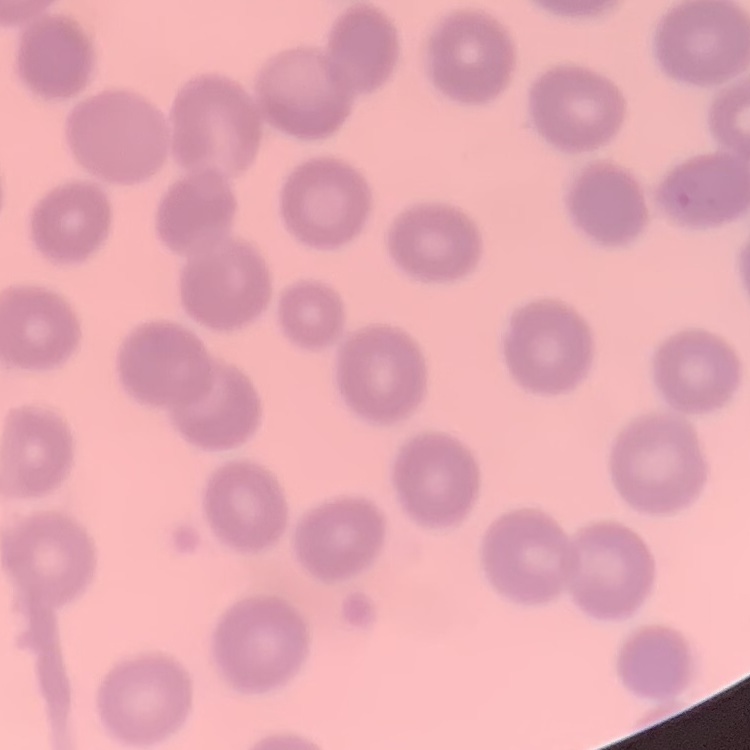

{
  "erythrocyte_morphology": "no rouleaux formation",
  "image_type": "one tile cut from a larger photomicrograph",
  "stain": "Field's or Giemsa",
  "preparation": "thin blood smear"
}